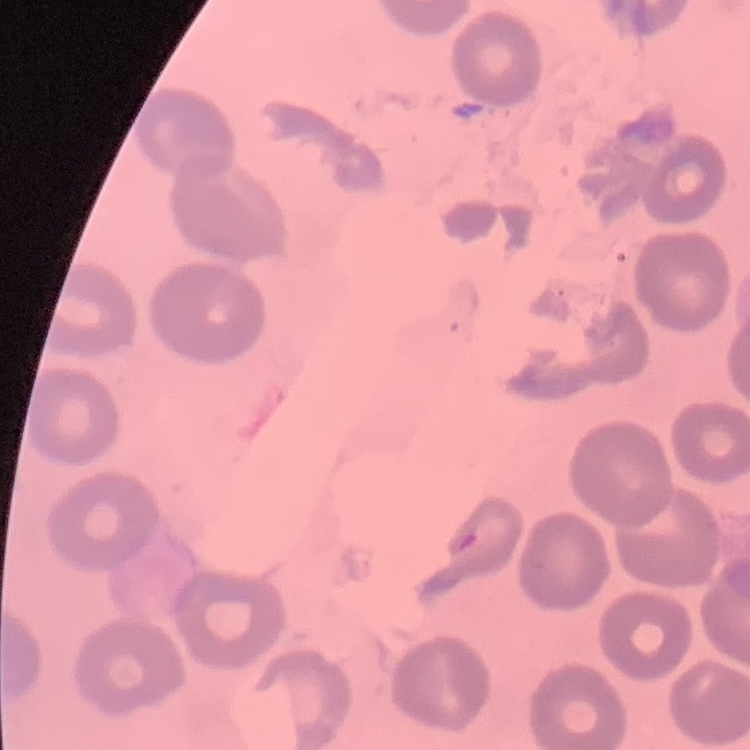
{
  "erythrocyte_morphology": "no rouleaux formation",
  "image_type": "square crop of a larger photomicrograph",
  "preparation": "thin blood smear",
  "stain": "Field's or Giemsa"
}